Assess this cell for malaria.
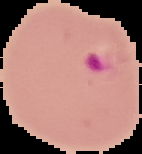
Parasitized.

image type = cell region segmented out of the field of view; surrounding area masked to black
image size = 142×154 pixels
preparation = thin blood smear